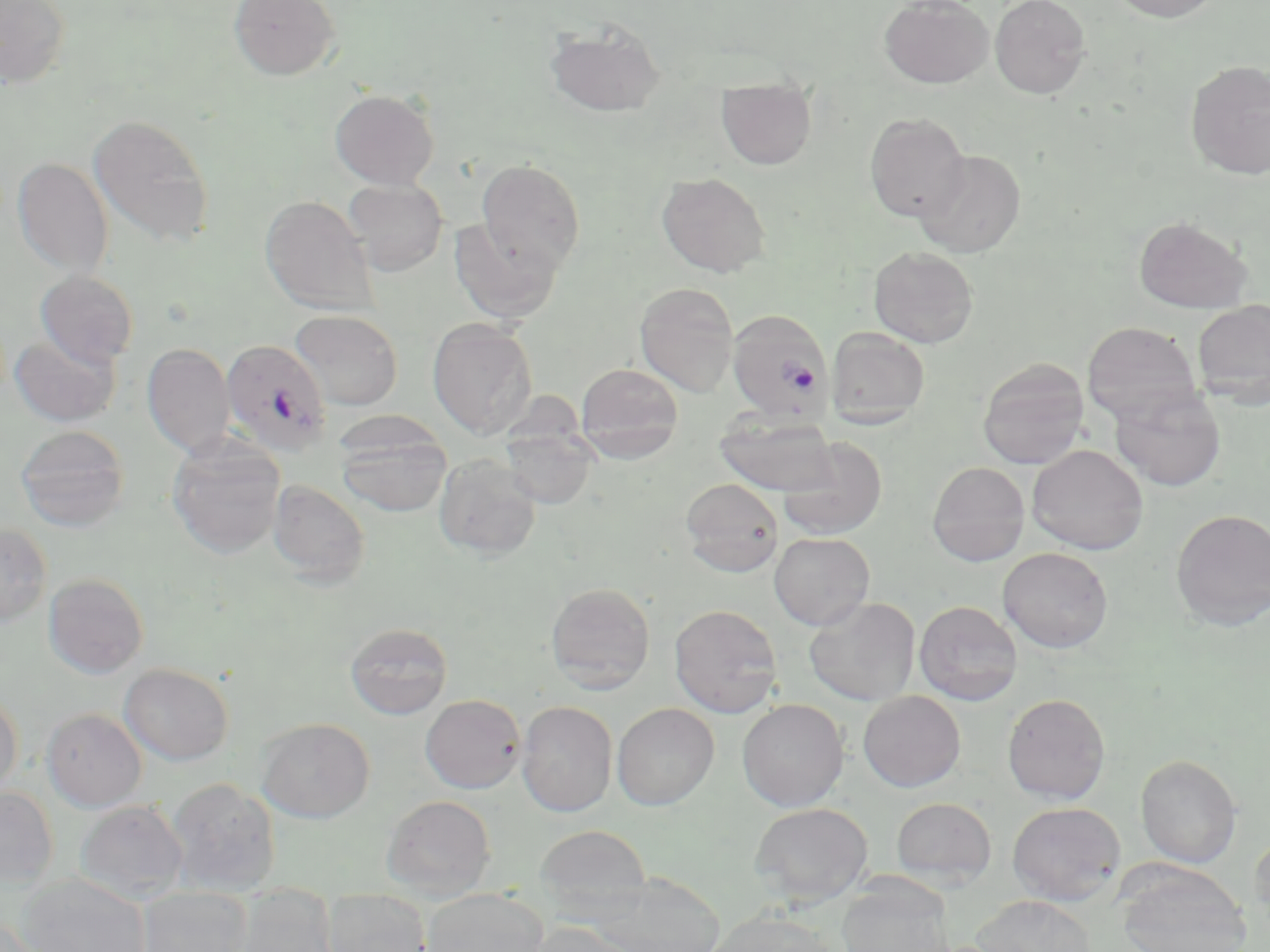
Approximate bounding boxes as named x1/y1/x2/y2 corners in pixels. Uninfected red blood cell locations: (x1=0, y1=0, x2=72, y2=88), (x1=229, y1=0, x2=340, y2=81), (x1=879, y1=0, x2=993, y2=89), (x1=990, y1=0, x2=1091, y2=99), (x1=1109, y1=0, x2=1223, y2=22), (x1=545, y1=20, x2=665, y2=118), (x1=1185, y1=60, x2=1270, y2=180), (x1=716, y1=79, x2=817, y2=170), (x1=329, y1=89, x2=439, y2=190), (x1=864, y1=112, x2=970, y2=222), (x1=87, y1=113, x2=214, y2=248), (x1=913, y1=149, x2=1026, y2=258), (x1=11, y1=157, x2=114, y2=278), (x1=476, y1=158, x2=585, y2=273), (x1=656, y1=171, x2=770, y2=277), (x1=342, y1=179, x2=448, y2=276), (x1=259, y1=196, x2=378, y2=316), (x1=1133, y1=216, x2=1253, y2=314), (x1=449, y1=218, x2=562, y2=324), (x1=868, y1=246, x2=978, y2=348), (x1=34, y1=270, x2=139, y2=368), (x1=634, y1=281, x2=739, y2=397), (x1=1192, y1=300, x2=1270, y2=408), (x1=290, y1=310, x2=404, y2=410), (x1=427, y1=318, x2=538, y2=439), (x1=1081, y1=321, x2=1203, y2=424), (x1=827, y1=326, x2=930, y2=428), (x1=10, y1=333, x2=121, y2=427), (x1=142, y1=343, x2=235, y2=458), (x1=977, y1=357, x2=1090, y2=469), (x1=575, y1=362, x2=685, y2=460), (x1=1109, y1=384, x2=1226, y2=492), (x1=715, y1=413, x2=840, y2=496), (x1=16, y1=425, x2=130, y2=531), (x1=335, y1=426, x2=452, y2=518), (x1=500, y1=426, x2=598, y2=509), (x1=777, y1=437, x2=888, y2=540), (x1=167, y1=439, x2=286, y2=558), (x1=1027, y1=444, x2=1148, y2=555), (x1=433, y1=455, x2=542, y2=560), (x1=927, y1=461, x2=1030, y2=566), (x1=680, y1=477, x2=784, y2=577), (x1=268, y1=479, x2=369, y2=587), (x1=1170, y1=508, x2=1270, y2=630), (x1=0, y1=522, x2=52, y2=626), (x1=769, y1=532, x2=875, y2=630), (x1=998, y1=547, x2=1113, y2=653), (x1=43, y1=573, x2=150, y2=678), (x1=545, y1=582, x2=655, y2=692), (x1=804, y1=597, x2=921, y2=706), (x1=914, y1=600, x2=1022, y2=706), (x1=669, y1=604, x2=783, y2=718), (x1=345, y1=622, x2=453, y2=720), (x1=119, y1=663, x2=233, y2=766), (x1=858, y1=690, x2=966, y2=792), (x1=0, y1=692, x2=23, y2=796), (x1=1002, y1=693, x2=1111, y2=804), (x1=420, y1=694, x2=526, y2=793), (x1=737, y1=698, x2=849, y2=811), (x1=516, y1=701, x2=618, y2=817), (x1=612, y1=702, x2=719, y2=810), (x1=42, y1=707, x2=147, y2=811), (x1=256, y1=717, x2=375, y2=823), (x1=1135, y1=754, x2=1242, y2=868), (x1=165, y1=777, x2=281, y2=896), (x1=0, y1=787, x2=58, y2=888), (x1=382, y1=794, x2=496, y2=900), (x1=891, y1=797, x2=997, y2=887), (x1=75, y1=800, x2=188, y2=904), (x1=1007, y1=801, x2=1125, y2=906), (x1=749, y1=802, x2=873, y2=907), (x1=534, y1=824, x2=652, y2=917), (x1=1249, y1=832, x2=1270, y2=934), (x1=1115, y1=863, x2=1252, y2=952), (x1=589, y1=872, x2=726, y2=952), (x1=17, y1=874, x2=151, y2=952), (x1=837, y1=874, x2=956, y2=952), (x1=232, y1=885, x2=338, y2=952), (x1=138, y1=887, x2=253, y2=952), (x1=422, y1=888, x2=548, y2=952), (x1=323, y1=889, x2=431, y2=952), (x1=971, y1=895, x2=1096, y2=952), (x1=706, y1=909, x2=840, y2=952), (x1=0, y1=915, x2=52, y2=951), (x1=522, y1=920, x2=641, y2=952). Plasmodium falciparum-infected red blood cell locations: (x1=727, y1=309, x2=834, y2=422), (x1=221, y1=339, x2=333, y2=456). Slide-level diagnosis: Plasmodium falciparum. Light microscopy. Captured at 1000x magnification. May-Grünwald-Giemsa-stained preparation. Thin blood film. Image is 1270×952 pixels. Single field of view.